Identify the cell.
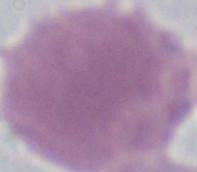

An erythrocyte.

Summary:
  - Magnification: 1000x
  - Modality: micrograph